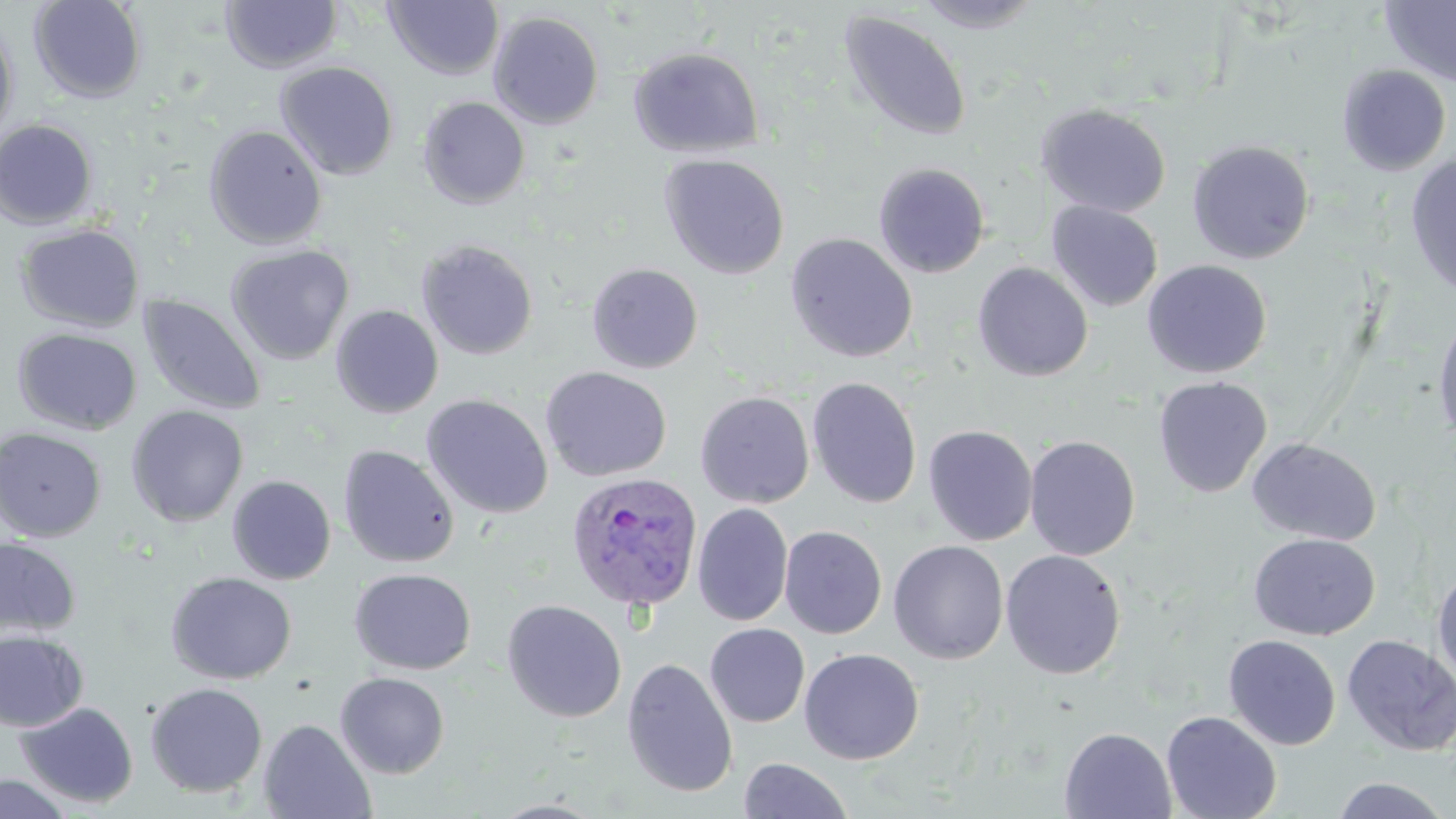

Summary:
  - Coordinate format: approximate bounding boxes as named x1/y1/x2/y2 corners in pixels
  - Plasmodium ovale-infected red blood cell locations: (x1=565, y1=471, x2=705, y2=613)
  - Uninfected red blood cell locations: (x1=28, y1=0, x2=147, y2=104), (x1=912, y1=0, x2=1045, y2=33), (x1=220, y1=1, x2=341, y2=74), (x1=383, y1=1, x2=504, y2=81), (x1=1381, y1=1, x2=1456, y2=87), (x1=488, y1=10, x2=605, y2=129), (x1=839, y1=10, x2=972, y2=143), (x1=0, y1=15, x2=19, y2=148), (x1=628, y1=47, x2=764, y2=159), (x1=275, y1=61, x2=399, y2=180), (x1=1337, y1=64, x2=1452, y2=176), (x1=418, y1=96, x2=530, y2=209), (x1=1036, y1=103, x2=1172, y2=218), (x1=0, y1=119, x2=99, y2=229), (x1=204, y1=124, x2=328, y2=249), (x1=1187, y1=139, x2=1315, y2=264), (x1=658, y1=153, x2=790, y2=280), (x1=1405, y1=154, x2=1456, y2=297), (x1=873, y1=162, x2=990, y2=278), (x1=1046, y1=202, x2=1163, y2=312), (x1=15, y1=223, x2=144, y2=333), (x1=784, y1=232, x2=918, y2=363), (x1=416, y1=239, x2=539, y2=360), (x1=226, y1=244, x2=354, y2=365), (x1=1142, y1=260, x2=1272, y2=379), (x1=586, y1=262, x2=704, y2=374), (x1=972, y1=262, x2=1094, y2=383), (x1=139, y1=295, x2=267, y2=416), (x1=330, y1=304, x2=444, y2=419), (x1=1432, y1=310, x2=1456, y2=446), (x1=13, y1=327, x2=143, y2=435), (x1=540, y1=366, x2=672, y2=482), (x1=1153, y1=376, x2=1272, y2=498), (x1=806, y1=377, x2=922, y2=509), (x1=695, y1=391, x2=814, y2=508), (x1=421, y1=394, x2=554, y2=519), (x1=125, y1=405, x2=249, y2=527), (x1=922, y1=424, x2=1038, y2=546), (x1=0, y1=426, x2=107, y2=543), (x1=1024, y1=435, x2=1140, y2=561), (x1=1246, y1=437, x2=1381, y2=546), (x1=337, y1=444, x2=459, y2=568), (x1=227, y1=475, x2=336, y2=585), (x1=692, y1=503, x2=793, y2=626), (x1=779, y1=525, x2=887, y2=639), (x1=1248, y1=532, x2=1379, y2=640), (x1=0, y1=537, x2=81, y2=641), (x1=888, y1=540, x2=1009, y2=664), (x1=1000, y1=549, x2=1126, y2=679), (x1=1432, y1=564, x2=1456, y2=689), (x1=349, y1=567, x2=477, y2=675), (x1=166, y1=571, x2=297, y2=685), (x1=501, y1=599, x2=628, y2=723), (x1=704, y1=623, x2=810, y2=727), (x1=0, y1=629, x2=88, y2=733), (x1=1341, y1=634, x2=1456, y2=757), (x1=1223, y1=635, x2=1341, y2=750), (x1=798, y1=648, x2=924, y2=765), (x1=621, y1=657, x2=738, y2=798), (x1=335, y1=672, x2=449, y2=778), (x1=145, y1=682, x2=268, y2=798), (x1=16, y1=701, x2=138, y2=808), (x1=1161, y1=710, x2=1282, y2=819), (x1=258, y1=718, x2=376, y2=819), (x1=1059, y1=727, x2=1177, y2=818), (x1=738, y1=757, x2=853, y2=818), (x1=0, y1=773, x2=73, y2=818), (x1=1330, y1=776, x2=1450, y2=818)
  - Slide-level diagnosis: Plasmodium ovale
  - Stain: May-Grünwald-Giemsa
  - Image size: 1456×819 pixels
  - Field of view: single
  - Magnification: 1000x
  - Preparation: thin blood film
  - Modality: light microscopy